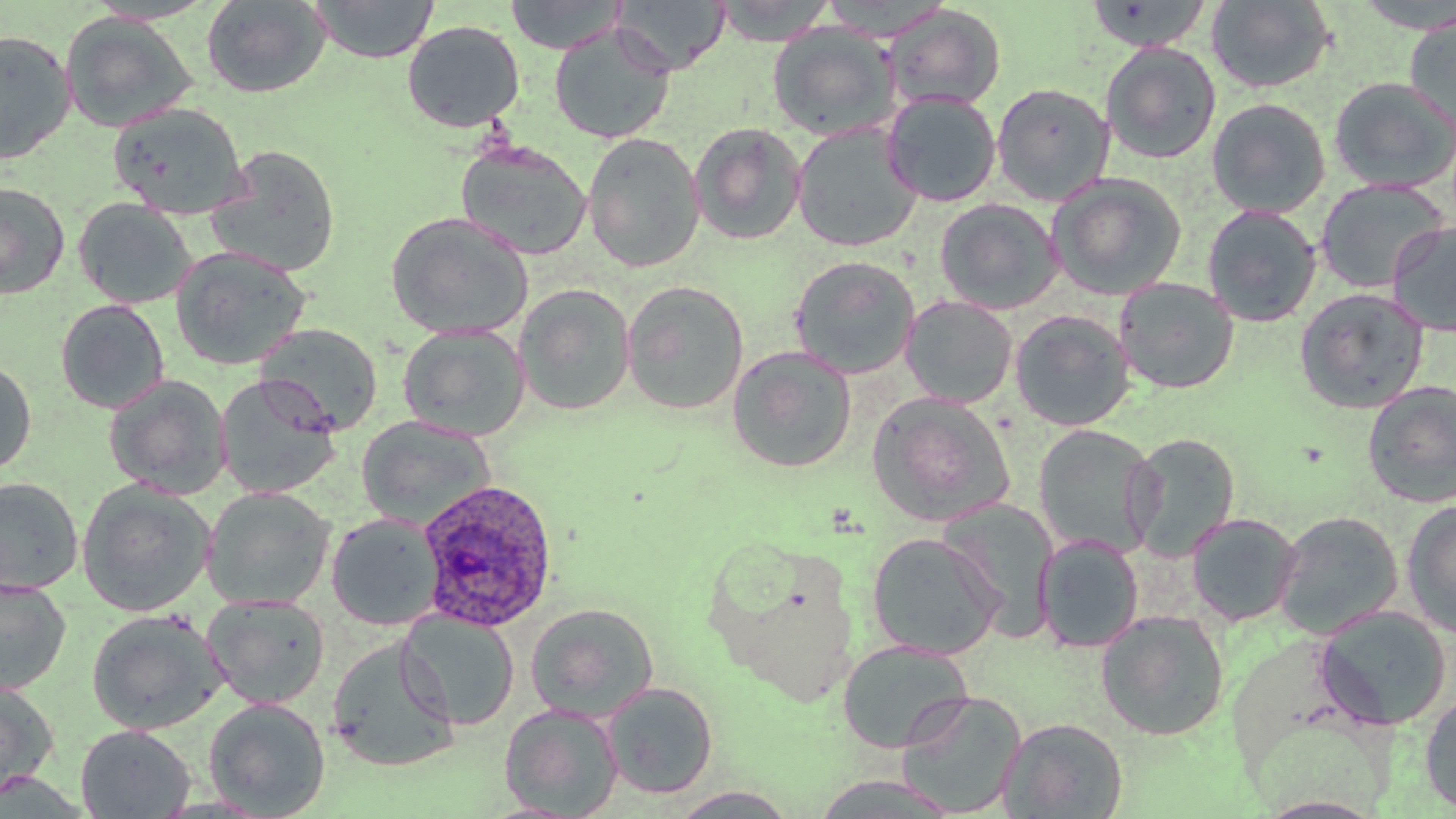

Approximate bounding boxes as [x1, y1, x2, y2] in pixels. Uninfected red blood cell locations: [201, 0, 331, 98], [312, 0, 438, 63], [504, 0, 626, 54], [612, 0, 731, 75], [712, 0, 837, 46], [1085, 0, 1213, 52], [1351, 0, 1456, 32], [1206, 1, 1336, 94], [884, 4, 1006, 112], [1404, 11, 1456, 138], [59, 12, 198, 134], [401, 20, 525, 133], [767, 22, 898, 141], [549, 25, 676, 144], [0, 29, 76, 165], [1100, 42, 1221, 164], [1329, 77, 1456, 193], [992, 82, 1115, 206], [882, 93, 1001, 207], [1206, 98, 1331, 218], [108, 103, 249, 218], [689, 122, 807, 245], [791, 123, 922, 252], [582, 132, 705, 273], [456, 141, 592, 261], [205, 145, 342, 277], [1047, 173, 1187, 301], [1315, 178, 1450, 293], [0, 182, 70, 299], [72, 198, 197, 309], [935, 198, 1063, 315], [1201, 204, 1322, 328], [385, 211, 534, 340], [1387, 220, 1455, 337], [170, 245, 312, 371], [790, 256, 920, 379], [1113, 277, 1239, 394], [622, 280, 749, 415], [514, 283, 636, 416], [1294, 287, 1430, 413], [900, 295, 1018, 408], [55, 299, 170, 414], [1010, 310, 1136, 432], [255, 322, 384, 436], [398, 323, 530, 441], [727, 346, 857, 473], [0, 358, 37, 475], [104, 374, 232, 498], [215, 376, 342, 499], [1361, 380, 1456, 508], [866, 391, 1015, 526], [357, 416, 496, 528], [1033, 424, 1160, 559], [1125, 432, 1241, 561], [0, 476, 83, 595], [77, 480, 215, 616], [202, 487, 335, 610], [937, 496, 1061, 640], [1401, 500, 1456, 638], [1273, 511, 1404, 639], [327, 512, 444, 630], [1185, 513, 1302, 627], [866, 532, 1005, 660], [1035, 534, 1144, 653], [0, 577, 71, 695], [201, 594, 331, 709], [525, 602, 660, 721], [1313, 605, 1452, 730], [87, 609, 227, 735], [397, 610, 520, 730], [1095, 610, 1230, 741], [326, 636, 460, 772], [836, 639, 972, 754], [0, 678, 58, 799], [602, 681, 718, 799], [897, 690, 1026, 816], [1419, 691, 1456, 816], [204, 697, 331, 818], [499, 703, 624, 818], [998, 716, 1128, 818], [75, 724, 195, 818], [809, 775, 962, 817], [668, 787, 802, 817]. Plasmodium ovale-infected red blood cell locations: [416, 479, 559, 632]. Slide-level diagnosis: Plasmodium ovale. Image is 1456×819 pixels. One field of a larger specimen. Optical microscopy. Captured at 1000x magnification. Thin blood smear. May-Grünwald-Giemsa stain.